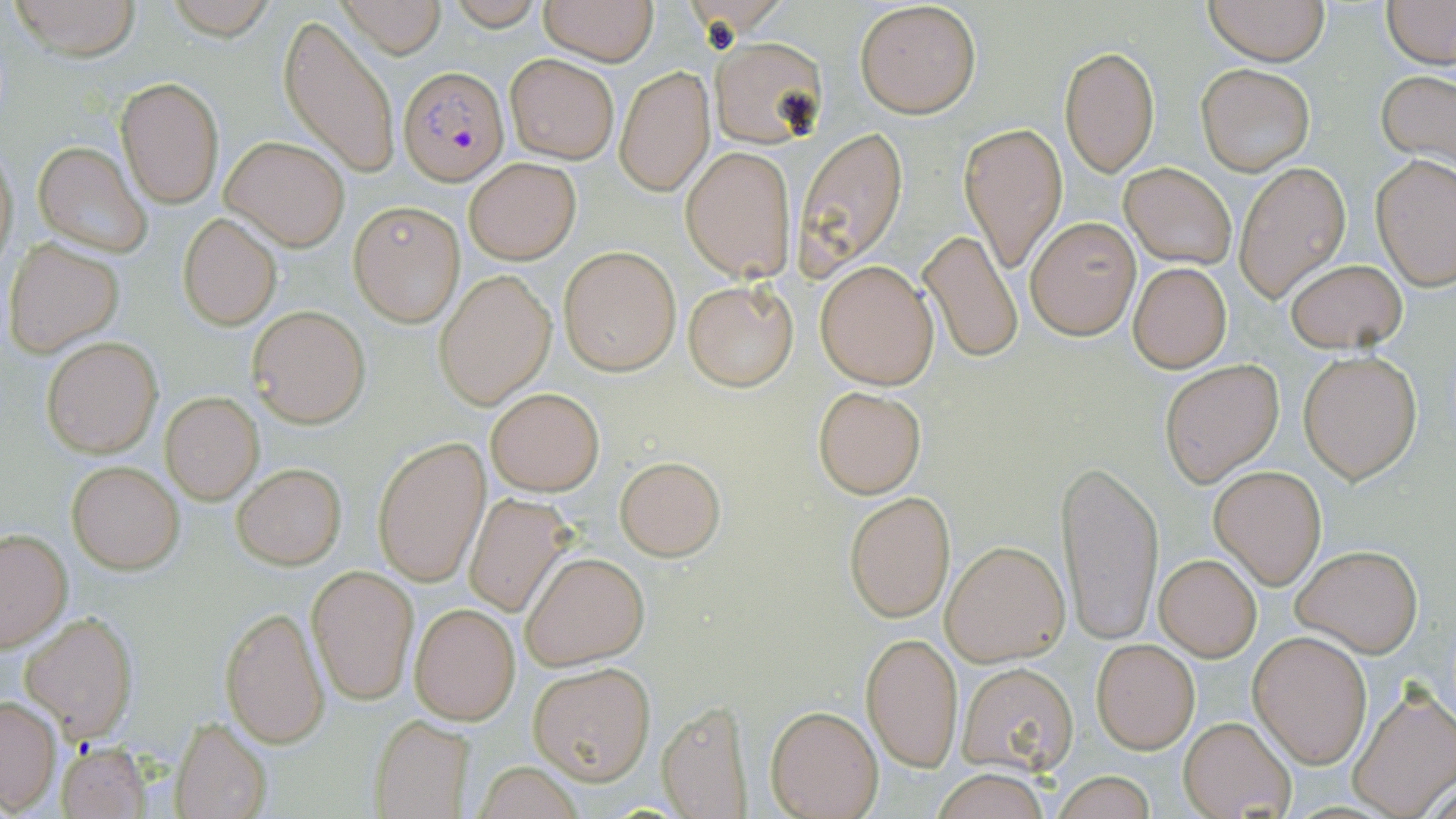

Plasmodium falciparum-infected red blood cell locations = approximate bounding boxes as named x1/y1/x2/y2 corners in pixels: (x1=401, y1=65, x2=506, y2=187)
slide-level diagnosis = Plasmodium falciparum
preparation = thin blood film
field of view = single
modality = light microscopy
image size = 1456×819 pixels
uninfected red blood cell locations = approximate bounding boxes as named x1/y1/x2/y2 corners in pixels: (x1=8, y1=0, x2=143, y2=61), (x1=166, y1=0, x2=275, y2=41), (x1=446, y1=0, x2=547, y2=31), (x1=538, y1=0, x2=658, y2=65), (x1=1202, y1=0, x2=1331, y2=66), (x1=335, y1=1, x2=447, y2=57), (x1=855, y1=1, x2=982, y2=118), (x1=1382, y1=1, x2=1455, y2=68), (x1=278, y1=15, x2=402, y2=181), (x1=710, y1=35, x2=827, y2=149), (x1=1061, y1=44, x2=1159, y2=176), (x1=505, y1=53, x2=620, y2=164), (x1=1196, y1=63, x2=1315, y2=174), (x1=615, y1=64, x2=714, y2=198), (x1=1377, y1=70, x2=1456, y2=173), (x1=117, y1=76, x2=224, y2=208), (x1=960, y1=121, x2=1066, y2=275), (x1=795, y1=127, x2=909, y2=271), (x1=221, y1=136, x2=350, y2=250), (x1=0, y1=139, x2=18, y2=273), (x1=33, y1=141, x2=152, y2=256), (x1=680, y1=145, x2=795, y2=281), (x1=1372, y1=154, x2=1455, y2=289), (x1=464, y1=158, x2=580, y2=264), (x1=1236, y1=161, x2=1351, y2=302), (x1=1119, y1=164, x2=1236, y2=270), (x1=350, y1=202, x2=464, y2=326), (x1=178, y1=213, x2=281, y2=331), (x1=1026, y1=218, x2=1139, y2=339), (x1=918, y1=230, x2=1022, y2=364), (x1=5, y1=239, x2=123, y2=356), (x1=558, y1=245, x2=681, y2=375), (x1=1284, y1=257, x2=1407, y2=352), (x1=816, y1=258, x2=939, y2=389), (x1=1128, y1=261, x2=1232, y2=373), (x1=435, y1=270, x2=556, y2=409), (x1=683, y1=278, x2=798, y2=390), (x1=249, y1=306, x2=370, y2=427), (x1=41, y1=337, x2=162, y2=457), (x1=1298, y1=350, x2=1423, y2=483), (x1=1160, y1=360, x2=1283, y2=485), (x1=813, y1=385, x2=927, y2=498), (x1=486, y1=387, x2=604, y2=496), (x1=160, y1=393, x2=264, y2=504), (x1=373, y1=436, x2=489, y2=587), (x1=615, y1=454, x2=724, y2=560), (x1=1057, y1=460, x2=1163, y2=645), (x1=67, y1=461, x2=183, y2=573), (x1=231, y1=463, x2=347, y2=569), (x1=1210, y1=466, x2=1327, y2=588), (x1=845, y1=490, x2=955, y2=622), (x1=464, y1=493, x2=575, y2=616), (x1=0, y1=528, x2=73, y2=652), (x1=941, y1=539, x2=1071, y2=665), (x1=1293, y1=543, x2=1422, y2=656), (x1=521, y1=551, x2=648, y2=670), (x1=1155, y1=554, x2=1261, y2=662), (x1=308, y1=565, x2=418, y2=705), (x1=410, y1=603, x2=520, y2=724), (x1=220, y1=607, x2=329, y2=747), (x1=20, y1=613, x2=137, y2=739), (x1=1250, y1=631, x2=1372, y2=767), (x1=861, y1=633, x2=963, y2=772), (x1=1091, y1=638, x2=1199, y2=754), (x1=956, y1=661, x2=1079, y2=775), (x1=528, y1=662, x2=654, y2=783), (x1=1348, y1=687, x2=1455, y2=817), (x1=0, y1=695, x2=62, y2=814), (x1=657, y1=700, x2=751, y2=817), (x1=767, y1=705, x2=883, y2=818), (x1=373, y1=714, x2=473, y2=819), (x1=1178, y1=715, x2=1297, y2=819), (x1=171, y1=717, x2=273, y2=819), (x1=57, y1=740, x2=150, y2=819), (x1=470, y1=761, x2=586, y2=818), (x1=930, y1=768, x2=1056, y2=819), (x1=1050, y1=771, x2=1160, y2=819)
stain = May-Grünwald-Giemsa
magnification = 1000x